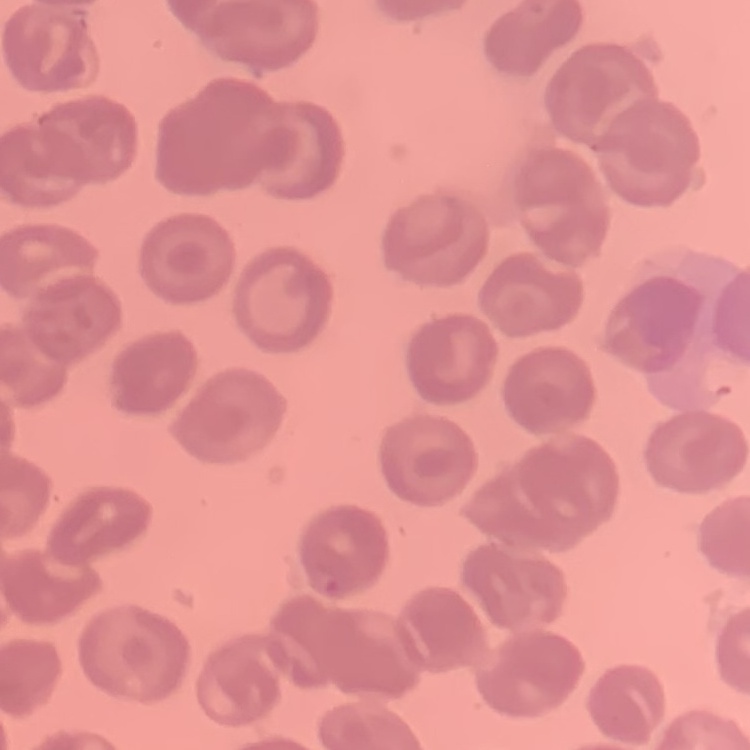

Summary:
  - Erythrocyte morphology: no rouleaux formation
  - Image type: one tile cut from a larger photomicrograph
  - Preparation: thin blood film
  - Stain: Field's or Giemsa